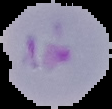

preparation = thin blood film
result = malaria parasites detected
image type = segmented cell region with the area outside set to black
image size = 112×109 pixels